Name the parasite shown.
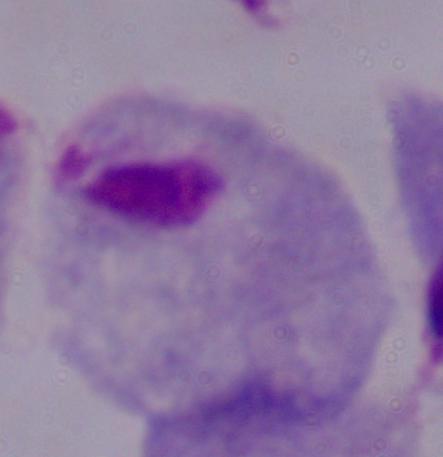

A trichomonad.

Summary:
  - Modality: micrograph
  - Magnification: 1000x